Report the malaria status of this cell.
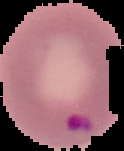
It is parasitized.

Summary:
  - Image size: 124×151 pixels
  - Image type: segmented cell region on a black background
  - Preparation: thin blood film